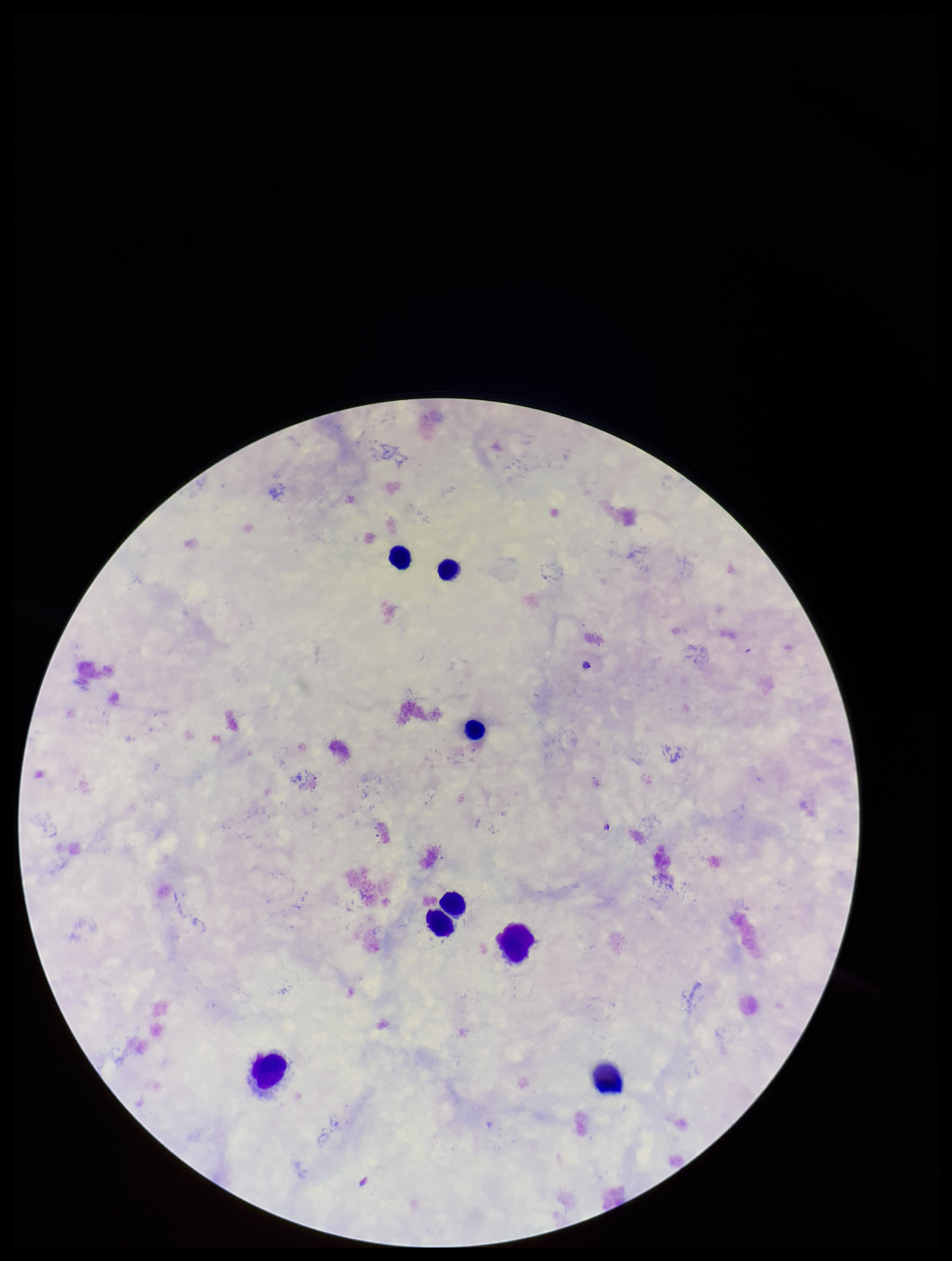

parasite_count: 0
stain: Giemsa
species_reported_for_this_patient: Plasmodium falciparum
capture: smartphone photograph through the microscope eyepiece
leukocyte_count: 8
preparation: thick
image_size: 952×1261 pixels
field_of_view: single
patient_malaria_status: infected
plasmodium_parasites: none identified